Locate every blood parasite and identify its species.
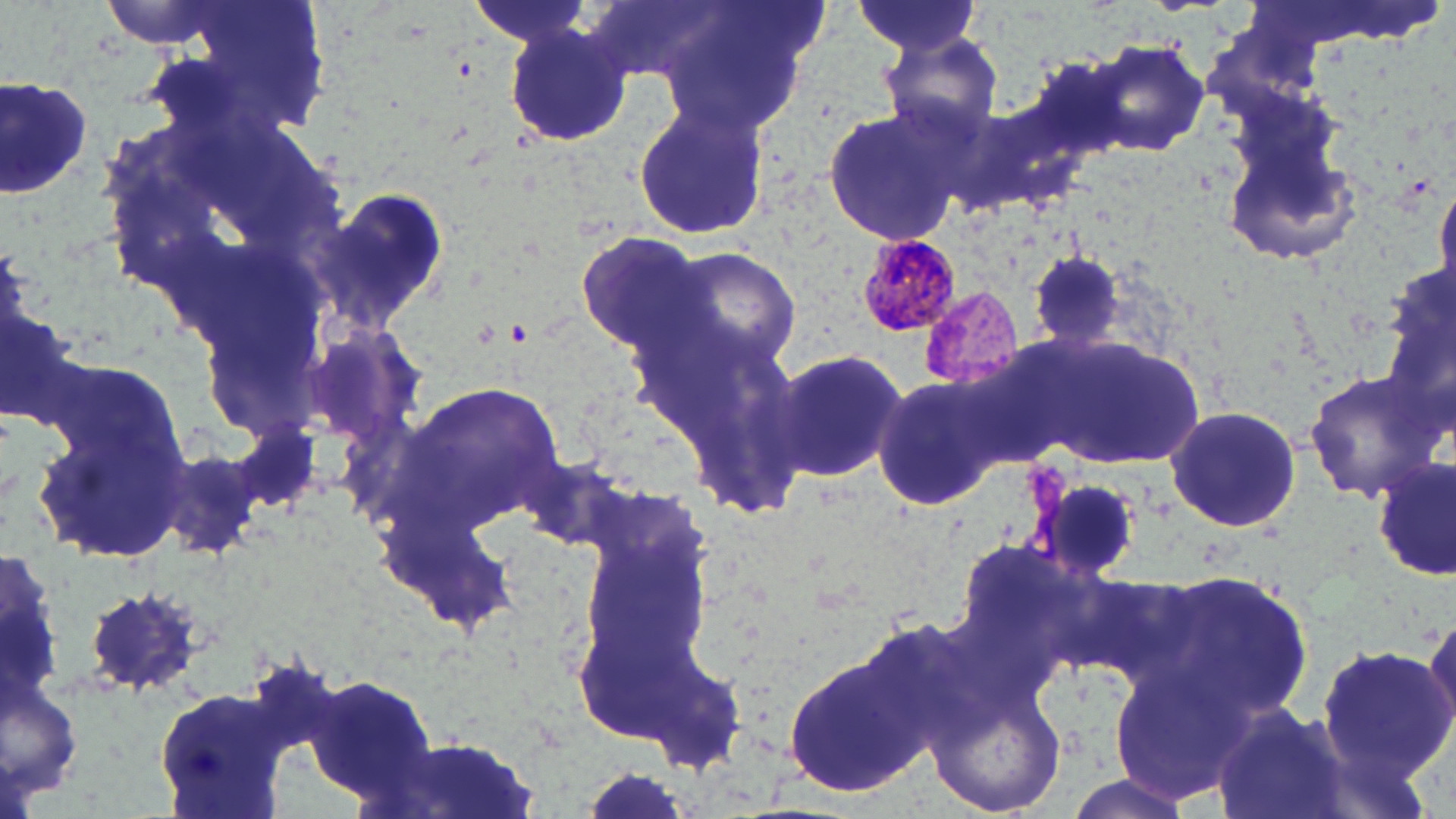

Approximate bounding boxes as [x1, y1, x2, y2] in pixels.
Plasmodium malariae-infected red blood cells: [853, 231, 962, 338].
No Plasmodium falciparum, Plasmodium ovale, Plasmodium vivax, Babesia divergens, or Trypanosoma brucei observed.

Summary:
  - Uninfected red blood cell locations: [95, 0, 241, 49], [142, 0, 339, 144], [657, 0, 816, 137], [463, 1, 600, 54], [850, 2, 985, 58], [503, 20, 633, 150], [879, 33, 1004, 141], [1086, 39, 1211, 158], [0, 73, 95, 201], [631, 99, 770, 243], [821, 105, 970, 248], [1223, 129, 1367, 271], [1429, 178, 1456, 303], [318, 189, 451, 332], [573, 231, 709, 355], [657, 245, 805, 372], [1026, 252, 1127, 352], [1382, 263, 1456, 415], [0, 304, 86, 431], [637, 314, 809, 517], [1031, 331, 1211, 469], [768, 345, 907, 485], [1303, 369, 1444, 504], [31, 374, 192, 567], [870, 375, 1006, 511], [395, 377, 565, 537], [1165, 403, 1304, 535], [228, 413, 323, 521], [512, 452, 640, 559], [1374, 456, 1455, 582], [1136, 570, 1319, 723], [80, 586, 209, 696], [1421, 604, 1456, 751], [1317, 641, 1452, 783], [782, 648, 931, 799], [299, 673, 446, 812], [925, 678, 1068, 816], [150, 684, 293, 819], [1210, 702, 1349, 819], [382, 732, 542, 819], [1059, 772, 1200, 819]
  - Slide-level diagnosis: Plasmodium malariae
  - Stain: May-Grünwald-Giemsa
  - Field of view: single
  - Preparation: thin blood smear
  - Image size: 1456×819 pixels
  - Modality: light microscopy
  - Magnification: 1000x